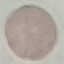
Summary:
  - Result: no malaria parasites seen
  - Stain: Giemsa
  - Capture: smartphone through the microscope eyepiece
  - Preparation: thin smear
  - Image type: cell patch, automatically extracted from a larger field of view and resized to 64 × 64 pixels